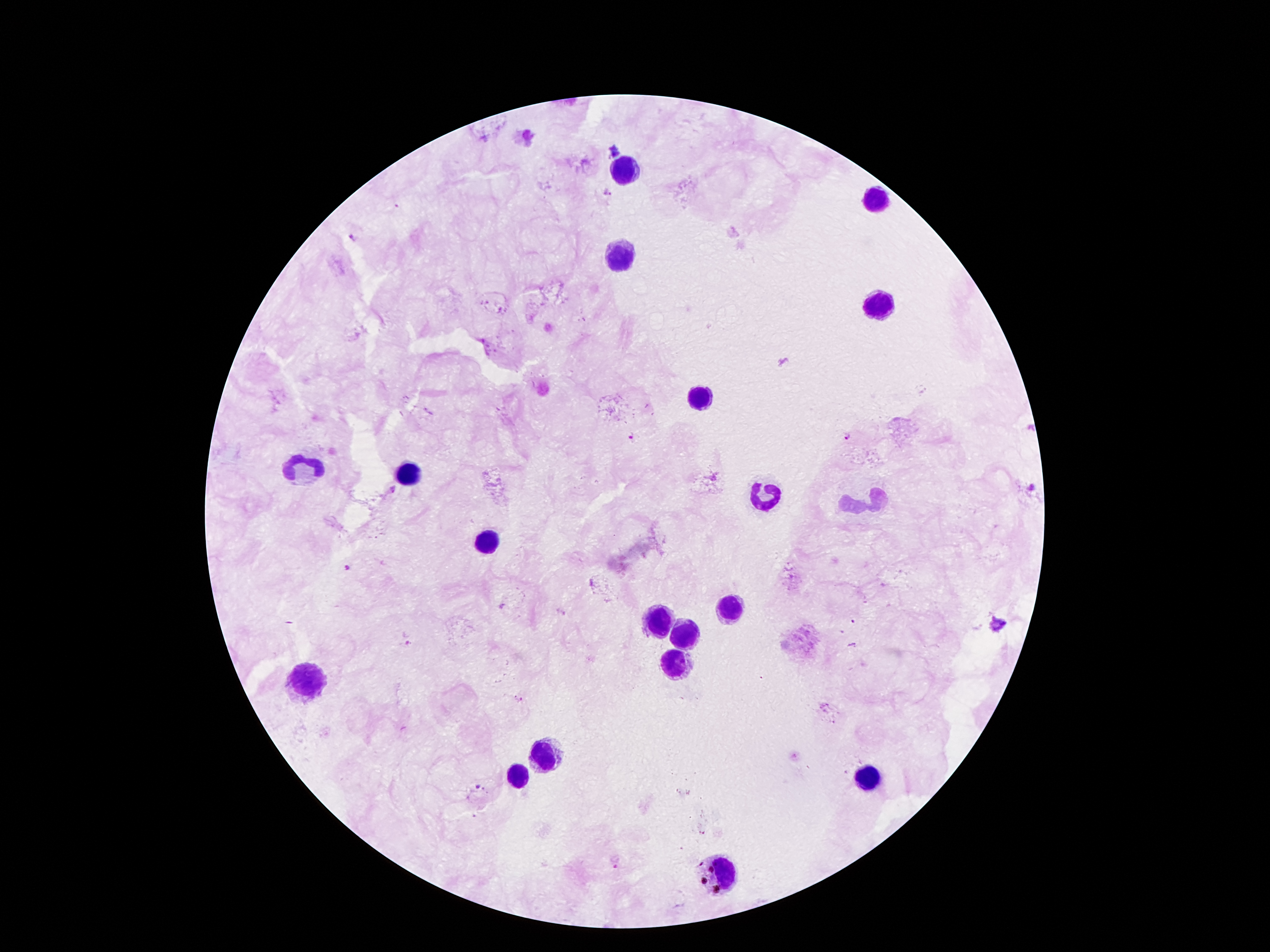 Approximate centers as [x, y] in pixels. Leukocyte locations: [626, 172], [874, 198], [621, 256], [876, 303], [703, 397], [307, 468], [409, 473], [769, 492], [874, 502], [489, 540], [727, 607], [657, 620], [684, 635], [676, 658], [304, 676], [546, 756], [519, 773], [867, 777], [720, 874]. Plasmodium parasite locations: [615, 148], [610, 192], [352, 237], [633, 434], [845, 436], [392, 491], [348, 568], [997, 624], [516, 697], [479, 787]. Patient malaria status: infected with Plasmodium falciparum. Giemsa-stained preparation. Single field of view. 100x magnification. Image is 1270×952 pixels. Photographed through the microscope eyepiece with a smartphone camera. Thick peripheral-blood smear.